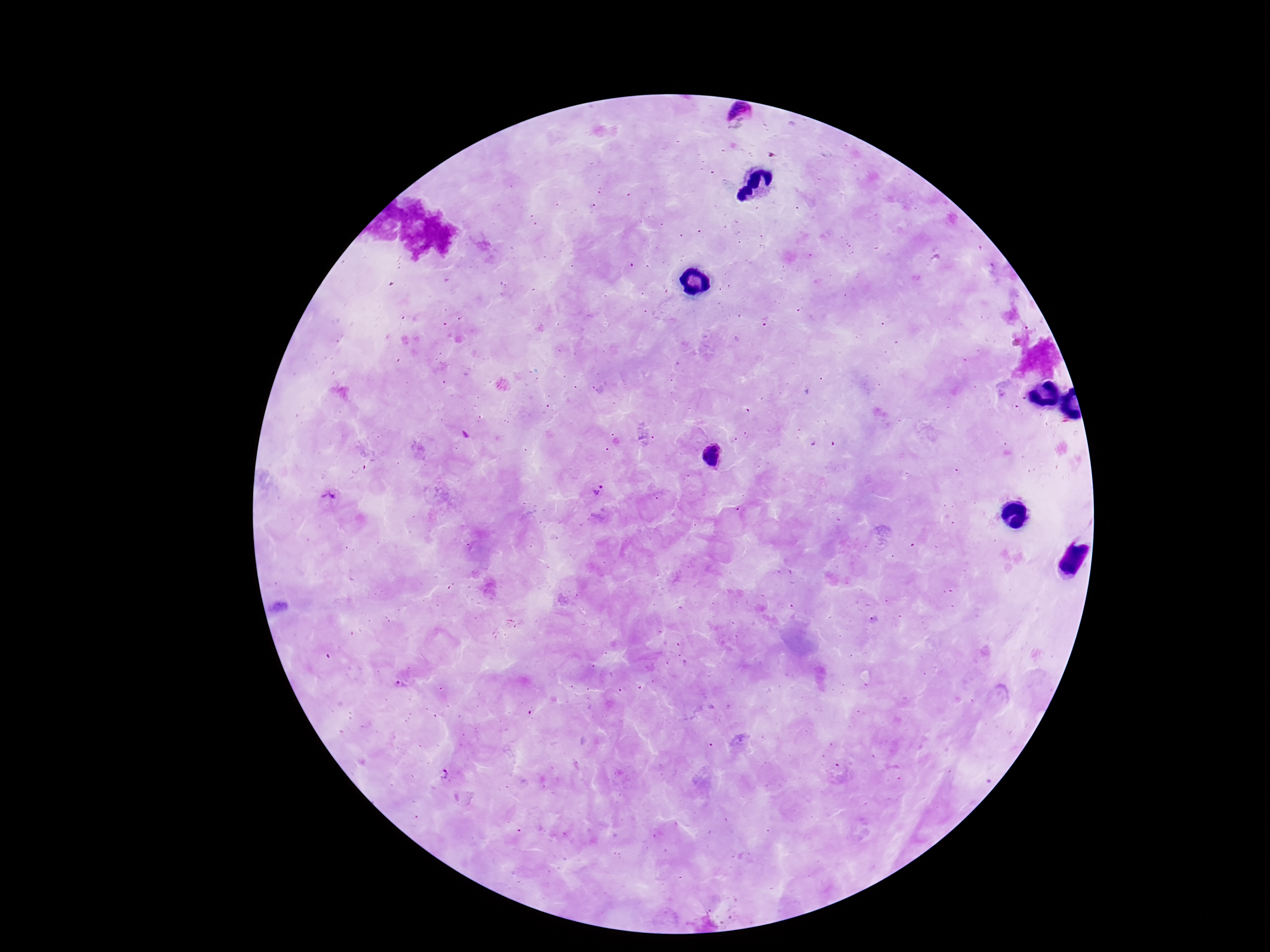
Plasmodium parasite locations = approximate centers as {x, y} in pixels: {737, 114}, {714, 457}, {599, 493}, {329, 499}, {401, 682}, {444, 774}
preparation = thick blood film
image size = 1270×952 pixels
capture = smartphone camera through the microscope eyepiece
stain = Giemsa
magnification = 100x
field of view = one from this slide
patient malaria status = positive